Locate every Plasmodium falciparum-infected red blood cell.
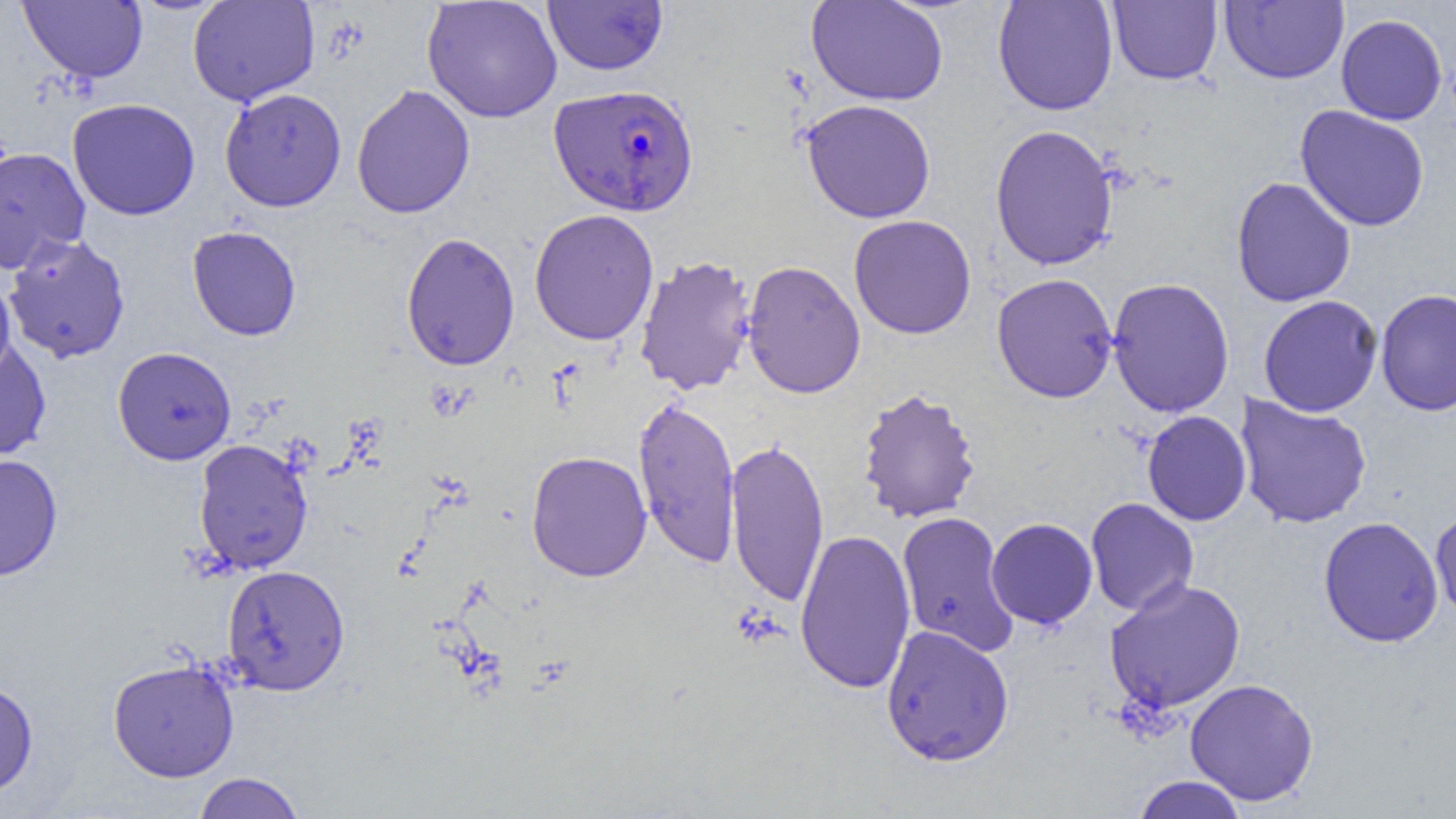
Approximate bounding boxes as (x1, y1, x2, y2) in pixels.
Plasmodium falciparum-infected red blood cells: (549, 83, 699, 216).

Uninfected red blood cell locations: (18, 0, 148, 83), (188, 0, 319, 107), (422, 0, 563, 124), (542, 0, 669, 76), (806, 0, 949, 106), (992, 0, 1118, 116), (1108, 0, 1222, 85), (1219, 1, 1349, 84), (1336, 14, 1448, 125), (351, 84, 476, 219), (219, 88, 347, 212), (67, 97, 201, 220), (801, 99, 937, 224), (1295, 105, 1430, 232), (990, 124, 1118, 270), (0, 146, 90, 274), (1230, 176, 1357, 308), (529, 209, 659, 346), (849, 215, 977, 340), (187, 225, 302, 341), (3, 232, 131, 364), (400, 232, 521, 372), (634, 254, 757, 396), (741, 260, 866, 399), (992, 272, 1118, 402), (0, 276, 15, 384), (1106, 277, 1235, 418), (1375, 289, 1456, 416), (1258, 295, 1383, 417), (0, 340, 51, 464), (112, 346, 237, 465), (856, 388, 981, 524), (1234, 393, 1373, 530), (633, 395, 741, 569), (1142, 411, 1251, 526), (725, 437, 829, 608), (193, 439, 313, 574), (526, 450, 652, 582), (0, 453, 63, 581), (1085, 497, 1199, 616), (1431, 504, 1456, 622), (897, 511, 1019, 658), (1318, 516, 1444, 647), (986, 517, 1098, 629), (795, 528, 916, 695), (222, 564, 350, 696), (1104, 579, 1246, 713), (881, 624, 1015, 767), (108, 659, 239, 781), (1184, 678, 1320, 806), (0, 679, 38, 798), (192, 772, 306, 819), (1131, 775, 1249, 819). Slide-level diagnosis: Plasmodium falciparum. Thin blood smear. Optical microscopy. One field of a larger specimen. Image is 1456×819 pixels. 1000x magnification.